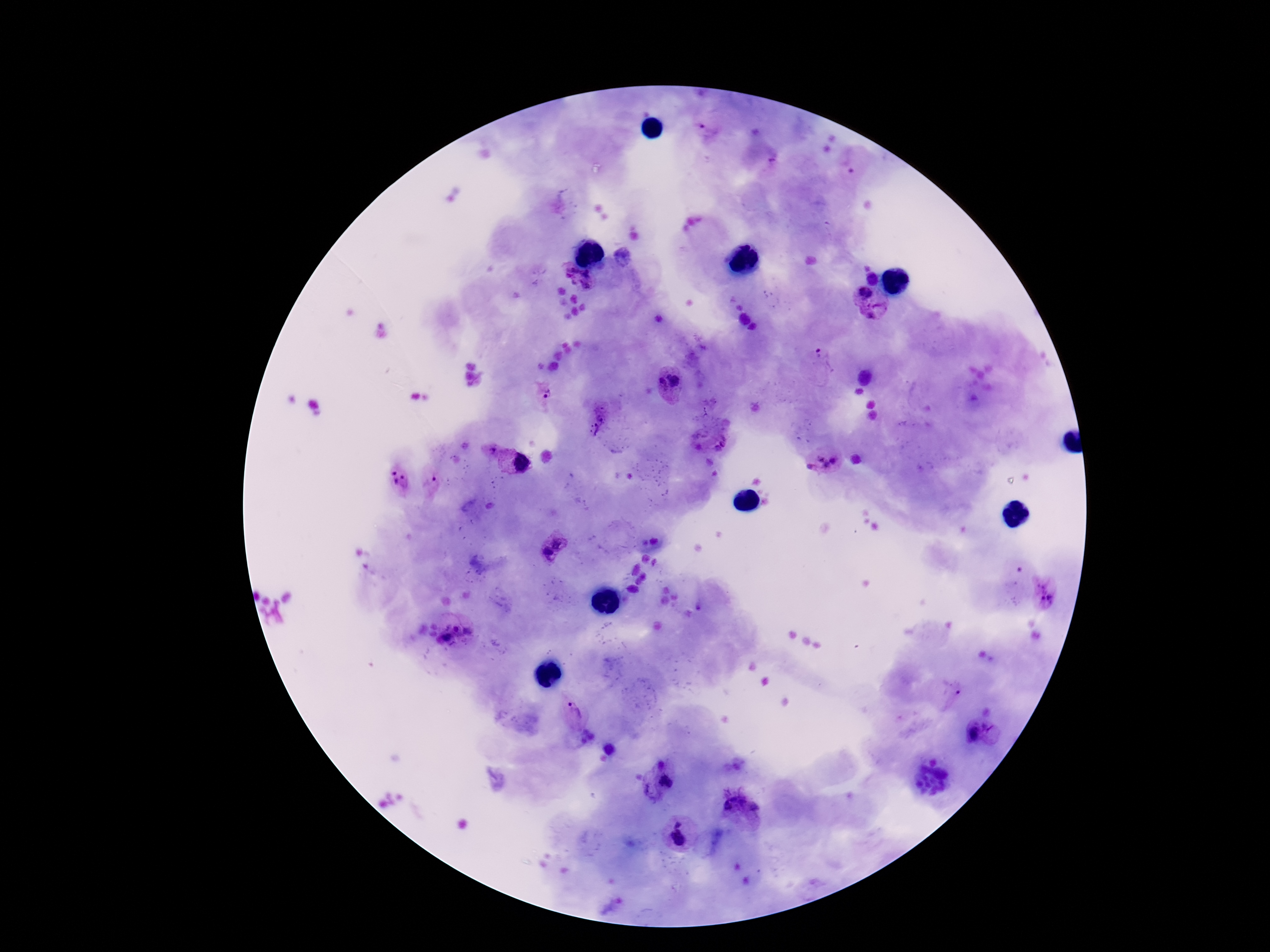

Approximate centers as (x, y) in pixels.
Summary:
  - Plasmodium parasite locations: (707, 130), (622, 258), (572, 267), (587, 274), (567, 278), (872, 278), (574, 283), (586, 286), (865, 292), (881, 304), (873, 315), (826, 359), (669, 381), (546, 392), (598, 425), (493, 450), (821, 458), (835, 459), (521, 462), (827, 464), (811, 467), (393, 472), (405, 477), (433, 479), (395, 482), (654, 541), (558, 542), (645, 542), (545, 556), (1044, 592), (455, 628), (468, 631), (446, 638), (955, 695), (575, 710), (989, 724), (974, 732), (662, 766), (666, 782), (649, 790), (734, 797), (745, 802), (726, 807), (756, 808), (678, 824), (678, 839)
  - Image size: 1270×952 pixels
  - Preparation: thick blood smear
  - Patient malaria status: positive
  - Magnification: 100x
  - Stain: Giemsa
  - Capture: smartphone camera through the microscope eyepiece
  - Field of view: single